Assess this cell for malaria.
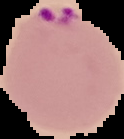

It is parasitized.

The area outside the segmented cell region is set to black. Image is 124×139 pixels. From a thin blood smear.